Assess this cell for malaria.
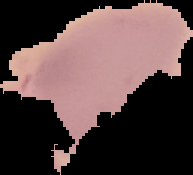

It is uninfected.

image type = segmented cell region on a black background
image size = 193×175 pixels
preparation = thin blood smear